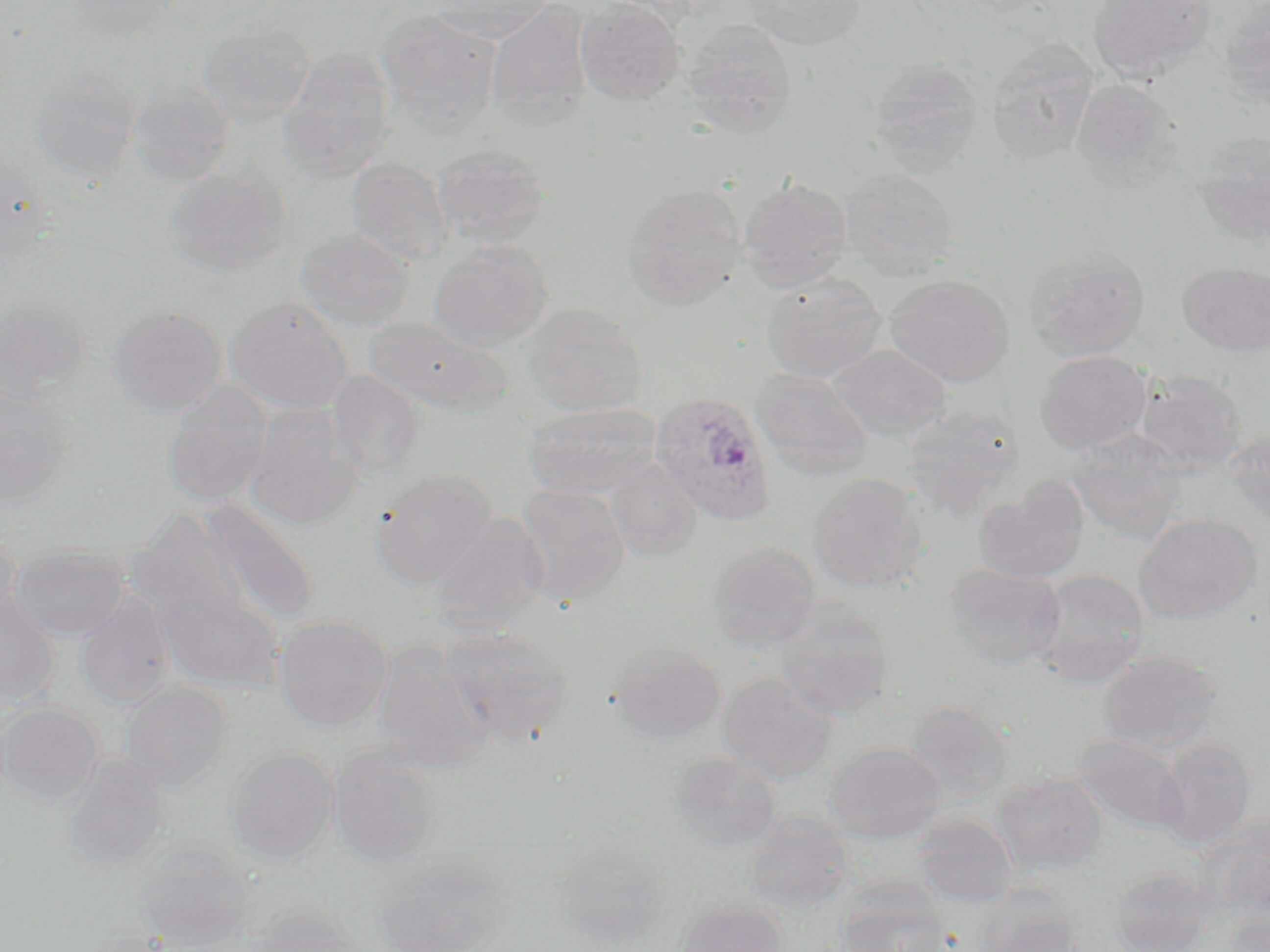
Summary:
  - Coordinate format: approximate bounding boxes as [x1, y1, x2, y2] in pixels
  - Plasmodium ovale-infected red blood cell locations: [649, 390, 777, 526]
  - Uninfected red blood cell locations: [63, 0, 178, 38], [430, 0, 554, 44], [486, 0, 593, 130], [575, 0, 685, 107], [744, 0, 866, 50], [1088, 0, 1217, 84], [1218, 4, 1270, 112], [375, 8, 503, 134], [683, 19, 798, 138], [199, 21, 316, 125], [987, 37, 1099, 164], [277, 46, 395, 184], [868, 56, 983, 175], [29, 66, 140, 184], [1071, 78, 1184, 190], [128, 83, 234, 187], [1190, 131, 1270, 245], [432, 143, 552, 250], [0, 154, 56, 263], [346, 156, 453, 266], [164, 163, 290, 277], [838, 168, 959, 278], [737, 177, 853, 291], [621, 183, 748, 311], [296, 228, 414, 329], [429, 240, 553, 351], [1023, 247, 1151, 361], [1178, 261, 1270, 357], [760, 272, 888, 384], [883, 274, 1015, 388], [225, 296, 354, 415], [0, 297, 91, 404], [523, 302, 647, 416], [107, 303, 227, 416], [364, 316, 515, 418], [828, 343, 952, 443], [1035, 350, 1151, 454], [750, 368, 874, 480], [1134, 368, 1248, 473], [327, 370, 425, 478], [161, 381, 274, 507], [0, 384, 77, 508], [522, 401, 663, 499], [244, 404, 363, 530], [901, 404, 1025, 519], [1223, 426, 1270, 530], [1066, 430, 1190, 544], [606, 457, 703, 561], [369, 469, 498, 589], [808, 473, 930, 592], [973, 480, 1089, 584], [515, 484, 630, 606], [197, 499, 320, 628], [128, 509, 251, 633], [427, 512, 550, 635], [1133, 513, 1263, 624], [0, 525, 20, 625], [705, 542, 822, 653], [9, 543, 132, 641], [942, 562, 1066, 670], [1030, 567, 1152, 687], [156, 584, 285, 693], [76, 589, 176, 708], [0, 590, 62, 707], [772, 598, 897, 720], [273, 614, 393, 732], [439, 626, 574, 747], [373, 637, 495, 772], [607, 641, 726, 745], [1096, 649, 1224, 754], [718, 673, 838, 785], [119, 681, 234, 790], [0, 701, 104, 805], [902, 701, 1014, 803], [1072, 734, 1187, 834], [1154, 738, 1257, 849], [824, 741, 946, 843], [327, 744, 444, 865], [227, 746, 339, 862], [666, 751, 782, 851], [61, 756, 172, 868], [992, 771, 1109, 873], [742, 810, 856, 913], [912, 813, 1019, 908], [1199, 817, 1270, 922], [552, 842, 672, 946], [137, 844, 258, 951], [371, 850, 512, 951], [1107, 864, 1217, 952], [836, 882, 951, 952], [973, 888, 1086, 952], [673, 898, 790, 952], [1224, 902, 1269, 952], [247, 905, 370, 952]
  - Slide-level diagnosis: Plasmodium ovale
  - Preparation: thin blood smear
  - Stain: May-Grünwald-Giemsa
  - Modality: light microscopy
  - Field of view: single
  - Magnification: 1000x
  - Image size: 1270×952 pixels